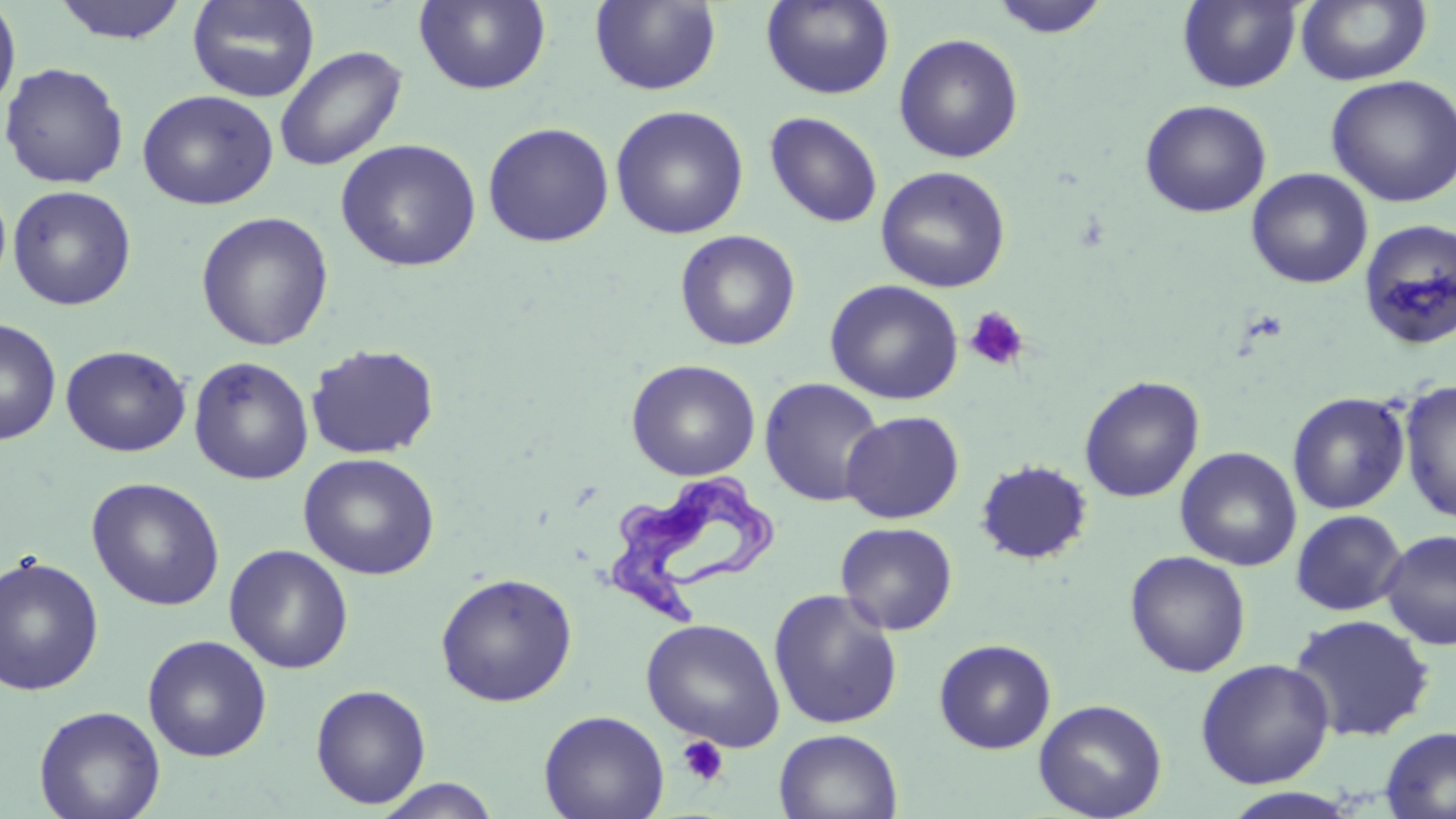
Approximate bounding boxes as named x1/y1/x2/y2 corners in pixels. Trypanosoma brucei locations: (x1=604, y1=475, x2=776, y2=630). Platelet locations: (x1=964, y1=306, x2=1030, y2=372), (x1=677, y1=736, x2=729, y2=787). Uninfected red blood cell locations: (x1=0, y1=0, x2=21, y2=120), (x1=52, y1=0, x2=190, y2=45), (x1=186, y1=0, x2=320, y2=103), (x1=414, y1=0, x2=551, y2=94), (x1=761, y1=0, x2=895, y2=99), (x1=989, y1=0, x2=1112, y2=39), (x1=589, y1=1, x2=722, y2=95), (x1=1178, y1=1, x2=1302, y2=93), (x1=1295, y1=1, x2=1431, y2=86), (x1=893, y1=33, x2=1024, y2=163), (x1=273, y1=45, x2=407, y2=171), (x1=1, y1=61, x2=130, y2=189), (x1=1325, y1=75, x2=1456, y2=207), (x1=137, y1=89, x2=279, y2=210), (x1=1139, y1=99, x2=1272, y2=218), (x1=610, y1=104, x2=749, y2=239), (x1=764, y1=111, x2=884, y2=228), (x1=482, y1=122, x2=615, y2=248), (x1=335, y1=138, x2=482, y2=272), (x1=875, y1=166, x2=1011, y2=293), (x1=1246, y1=168, x2=1373, y2=289), (x1=8, y1=185, x2=137, y2=310), (x1=196, y1=211, x2=334, y2=351), (x1=1358, y1=218, x2=1456, y2=350), (x1=674, y1=229, x2=801, y2=351), (x1=824, y1=279, x2=964, y2=405), (x1=0, y1=317, x2=62, y2=446), (x1=305, y1=343, x2=440, y2=460), (x1=60, y1=345, x2=191, y2=457), (x1=189, y1=356, x2=314, y2=485), (x1=625, y1=359, x2=761, y2=481), (x1=1079, y1=375, x2=1205, y2=503), (x1=759, y1=378, x2=886, y2=506), (x1=1399, y1=378, x2=1456, y2=524), (x1=1287, y1=391, x2=1411, y2=514), (x1=841, y1=410, x2=965, y2=524), (x1=1175, y1=446, x2=1302, y2=571), (x1=298, y1=452, x2=440, y2=580), (x1=975, y1=460, x2=1093, y2=565), (x1=86, y1=477, x2=225, y2=611), (x1=1291, y1=509, x2=1407, y2=616), (x1=835, y1=521, x2=958, y2=636), (x1=1379, y1=528, x2=1456, y2=651), (x1=224, y1=544, x2=354, y2=674), (x1=1125, y1=550, x2=1251, y2=677), (x1=0, y1=554, x2=104, y2=696), (x1=435, y1=572, x2=578, y2=707), (x1=767, y1=589, x2=904, y2=731), (x1=1288, y1=613, x2=1436, y2=742), (x1=641, y1=618, x2=786, y2=752), (x1=142, y1=634, x2=272, y2=762), (x1=934, y1=638, x2=1057, y2=754), (x1=1195, y1=658, x2=1335, y2=789), (x1=310, y1=684, x2=431, y2=809), (x1=1033, y1=698, x2=1168, y2=819), (x1=33, y1=705, x2=165, y2=819), (x1=538, y1=709, x2=669, y2=819), (x1=1380, y1=726, x2=1456, y2=819), (x1=774, y1=728, x2=902, y2=819), (x1=372, y1=778, x2=503, y2=818), (x1=1220, y1=787, x2=1363, y2=818). Slide-level diagnosis: Trypanosoma brucei. Single field of view. Image is 1456×819 pixels. Thin blood smear. 1000x magnification. Light microscopy. May-Grünwald-Giemsa-stained preparation.